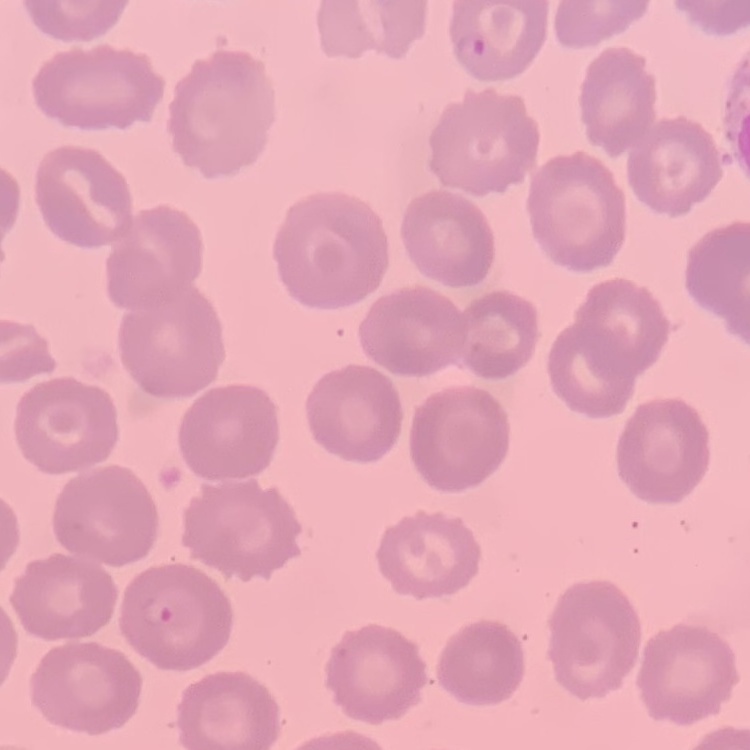

The erythrocytes exhibit no rouleaux formation. Stained with either Field's or Giemsa. Thin blood film. One tile cut from a larger photomicrograph.